Name the parasite shown.
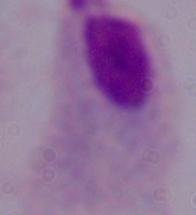

A trichomonad.

Micrograph. 1000x magnification.